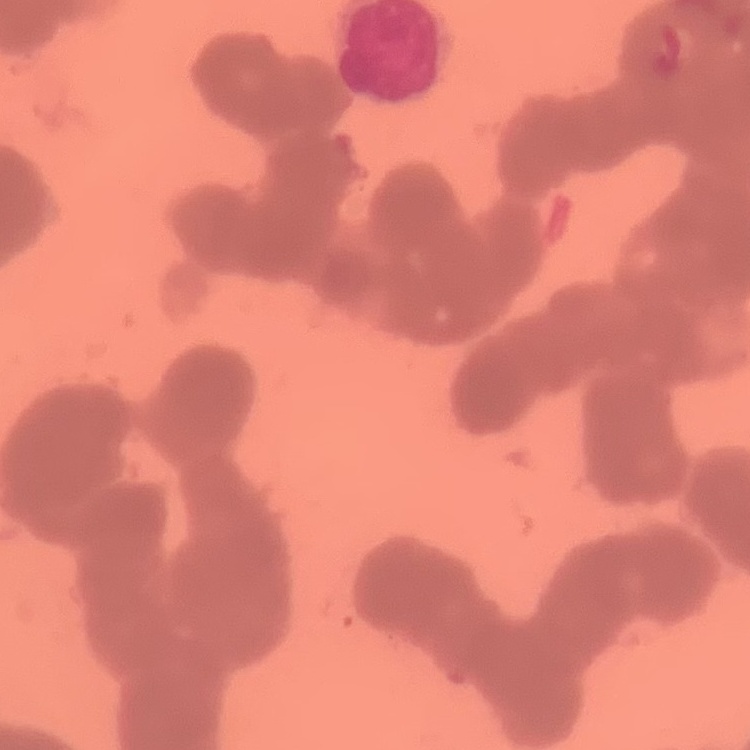
erythrocyte morphology = rouleaux formation
stain = Field's or Giemsa
preparation = thin peripheral smear
image type = square crop of a larger photomicrograph